Locate every blood parasite and identify its species.
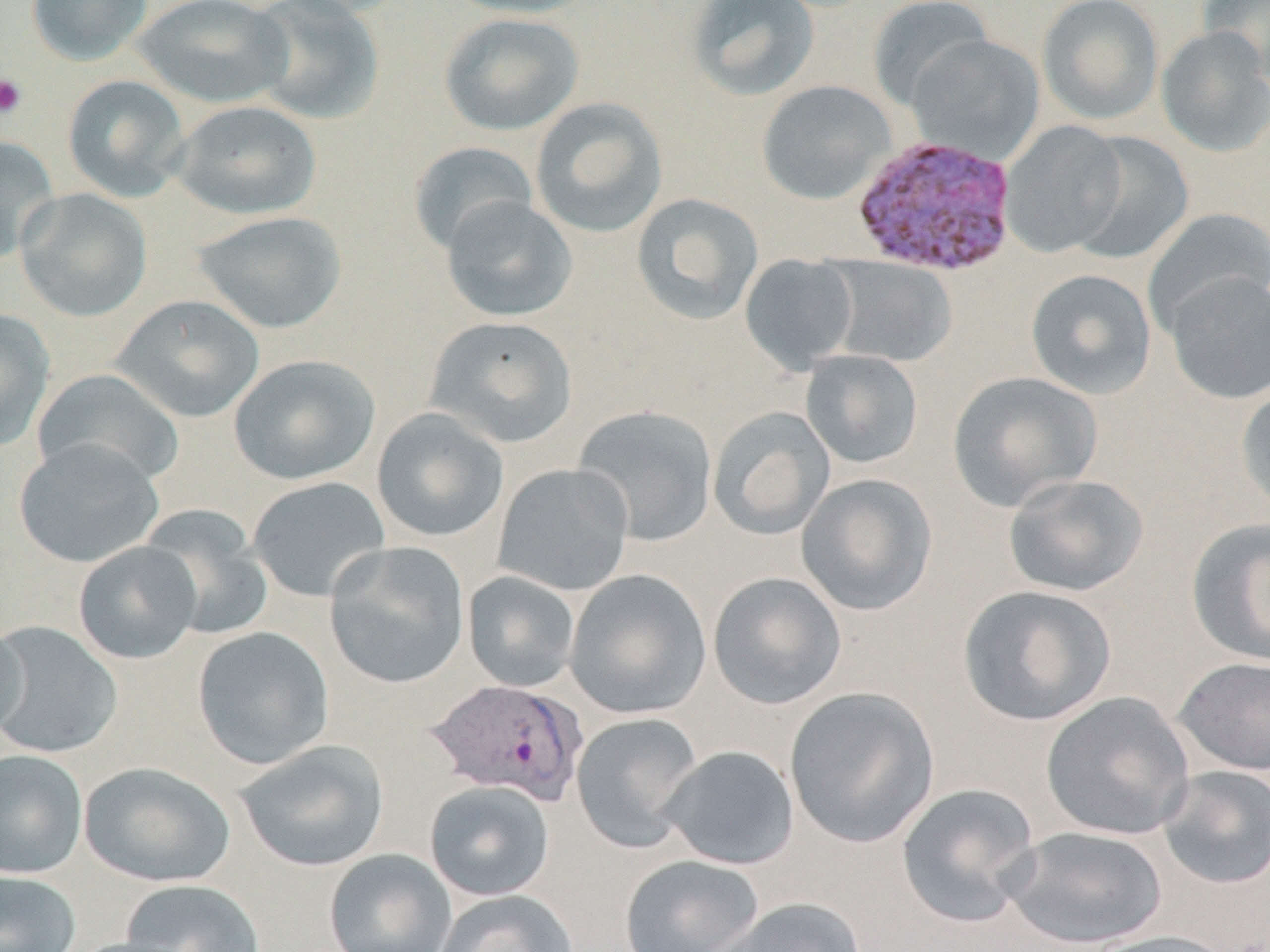
Approximate bounding boxes as named x1/y1/x2/y2 corners in pixels.
Plasmodium vivax-infected red blood cells: (x1=853, y1=132, x2=1022, y2=275), (x1=425, y1=678, x2=588, y2=805).
No Plasmodium falciparum, Plasmodium ovale, Plasmodium malariae, Babesia divergens, or Trypanosoma brucei observed.

Uninfected red blood cell locations: (x1=26, y1=0, x2=153, y2=65), (x1=131, y1=0, x2=293, y2=108), (x1=247, y1=0, x2=385, y2=125), (x1=442, y1=0, x2=597, y2=19), (x1=685, y1=0, x2=820, y2=101), (x1=868, y1=0, x2=995, y2=110), (x1=1037, y1=0, x2=1164, y2=125), (x1=1197, y1=0, x2=1270, y2=83), (x1=439, y1=12, x2=584, y2=136), (x1=1156, y1=26, x2=1270, y2=157), (x1=906, y1=35, x2=1044, y2=163), (x1=62, y1=74, x2=190, y2=202), (x1=757, y1=80, x2=896, y2=204), (x1=529, y1=97, x2=668, y2=238), (x1=170, y1=100, x2=322, y2=220), (x1=999, y1=120, x2=1128, y2=258), (x1=1071, y1=132, x2=1194, y2=264), (x1=0, y1=134, x2=60, y2=265), (x1=408, y1=141, x2=539, y2=256), (x1=15, y1=188, x2=152, y2=322), (x1=630, y1=192, x2=764, y2=326), (x1=440, y1=196, x2=578, y2=322), (x1=1142, y1=208, x2=1270, y2=334), (x1=191, y1=210, x2=348, y2=334), (x1=739, y1=254, x2=859, y2=373), (x1=828, y1=257, x2=957, y2=367), (x1=1025, y1=268, x2=1157, y2=400), (x1=1164, y1=272, x2=1270, y2=404), (x1=111, y1=294, x2=265, y2=423), (x1=0, y1=308, x2=55, y2=453), (x1=423, y1=315, x2=578, y2=448), (x1=799, y1=350, x2=924, y2=469), (x1=229, y1=354, x2=380, y2=485), (x1=33, y1=368, x2=184, y2=488), (x1=947, y1=370, x2=1102, y2=511), (x1=1235, y1=382, x2=1270, y2=517), (x1=573, y1=405, x2=719, y2=547), (x1=707, y1=406, x2=836, y2=541), (x1=372, y1=407, x2=508, y2=542), (x1=12, y1=438, x2=164, y2=568), (x1=493, y1=462, x2=634, y2=596), (x1=796, y1=473, x2=938, y2=616), (x1=1003, y1=473, x2=1149, y2=597), (x1=247, y1=476, x2=390, y2=602), (x1=138, y1=505, x2=273, y2=640), (x1=1186, y1=518, x2=1270, y2=666), (x1=73, y1=541, x2=202, y2=664), (x1=324, y1=541, x2=470, y2=689), (x1=564, y1=569, x2=712, y2=720), (x1=462, y1=571, x2=581, y2=693), (x1=708, y1=572, x2=847, y2=710), (x1=957, y1=584, x2=1117, y2=727), (x1=0, y1=613, x2=28, y2=744), (x1=0, y1=620, x2=122, y2=758), (x1=192, y1=626, x2=334, y2=770), (x1=1171, y1=655, x2=1270, y2=775), (x1=784, y1=686, x2=940, y2=848), (x1=1040, y1=691, x2=1195, y2=840), (x1=571, y1=712, x2=704, y2=853), (x1=235, y1=739, x2=389, y2=872), (x1=658, y1=745, x2=800, y2=870), (x1=0, y1=749, x2=88, y2=879), (x1=79, y1=761, x2=236, y2=887), (x1=1156, y1=765, x2=1270, y2=890), (x1=424, y1=779, x2=555, y2=901), (x1=895, y1=782, x2=1041, y2=928), (x1=1003, y1=825, x2=1168, y2=949), (x1=324, y1=848, x2=456, y2=952), (x1=619, y1=854, x2=764, y2=952), (x1=0, y1=869, x2=82, y2=952), (x1=118, y1=878, x2=265, y2=952), (x1=433, y1=889, x2=578, y2=952), (x1=707, y1=897, x2=869, y2=952), (x1=1083, y1=929, x2=1239, y2=952), (x1=65, y1=936, x2=196, y2=952). Platelet locations: (x1=0, y1=73, x2=28, y2=119). Slide-level diagnosis: Plasmodium vivax. May-Grünwald-Giemsa-stained preparation. Captured at 1000x magnification. Thin blood smear. One field of a larger specimen. Image is 1270×952 pixels. Light microscopy.